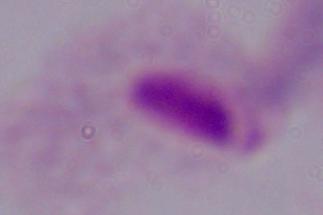
Summary:
  - Magnification: 1000x
  - Identification: trichomonad
  - Modality: photomicrograph